Locate every uninfected red blood cell.
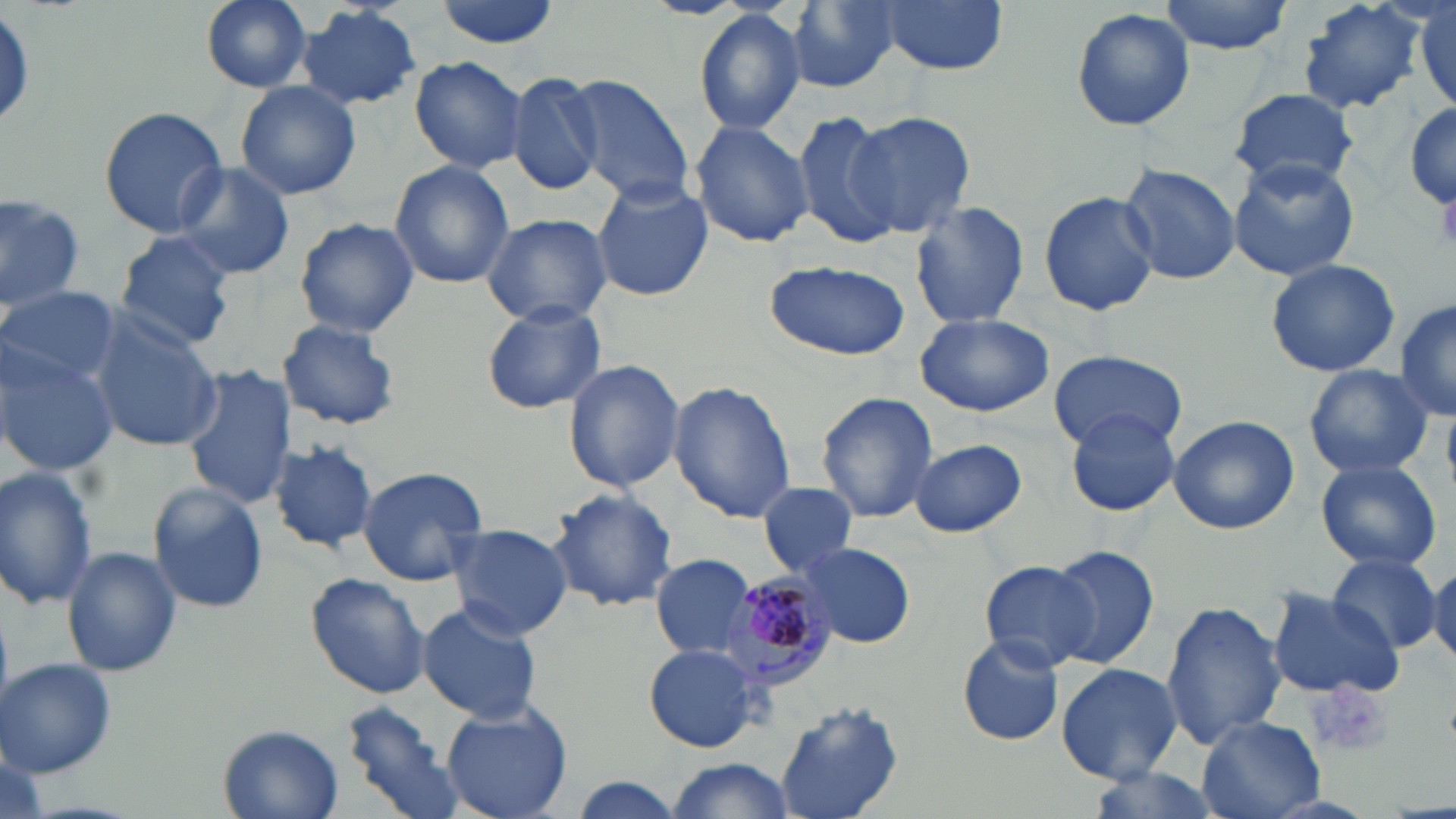
Approximate bounding boxes as named x1/y1/x2/y2 corners in pixels.
Uninfected red blood cells: (x1=197, y1=0, x2=315, y2=93), (x1=434, y1=0, x2=560, y2=49), (x1=639, y1=0, x2=756, y2=21), (x1=784, y1=0, x2=898, y2=93), (x1=877, y1=0, x2=1008, y2=74), (x1=1159, y1=0, x2=1293, y2=54), (x1=1295, y1=0, x2=1434, y2=116), (x1=1411, y1=2, x2=1454, y2=113), (x1=297, y1=4, x2=425, y2=110), (x1=1069, y1=7, x2=1196, y2=132), (x1=694, y1=10, x2=805, y2=133), (x1=408, y1=57, x2=528, y2=172), (x1=509, y1=72, x2=606, y2=197), (x1=559, y1=74, x2=695, y2=205), (x1=403, y1=77, x2=525, y2=260), (x1=233, y1=81, x2=362, y2=202), (x1=1229, y1=87, x2=1359, y2=191), (x1=1406, y1=103, x2=1456, y2=212), (x1=99, y1=106, x2=227, y2=237), (x1=795, y1=110, x2=903, y2=250), (x1=848, y1=112, x2=978, y2=238), (x1=690, y1=118, x2=814, y2=248), (x1=1228, y1=158, x2=1361, y2=281), (x1=387, y1=161, x2=515, y2=288), (x1=170, y1=163, x2=297, y2=280), (x1=1120, y1=164, x2=1241, y2=285), (x1=590, y1=177, x2=713, y2=302), (x1=1039, y1=189, x2=1160, y2=317), (x1=0, y1=192, x2=83, y2=311), (x1=911, y1=201, x2=1029, y2=330), (x1=480, y1=213, x2=613, y2=328), (x1=295, y1=217, x2=420, y2=337), (x1=112, y1=231, x2=237, y2=350), (x1=1265, y1=257, x2=1400, y2=378), (x1=765, y1=259, x2=911, y2=362), (x1=2, y1=285, x2=120, y2=389), (x1=1394, y1=295, x2=1455, y2=423), (x1=482, y1=300, x2=607, y2=414), (x1=87, y1=310, x2=224, y2=451), (x1=915, y1=310, x2=1055, y2=417), (x1=277, y1=319, x2=402, y2=430), (x1=1, y1=347, x2=118, y2=476), (x1=1049, y1=349, x2=1187, y2=453), (x1=562, y1=357, x2=685, y2=493), (x1=181, y1=364, x2=296, y2=510), (x1=1304, y1=364, x2=1433, y2=479), (x1=668, y1=380, x2=796, y2=523), (x1=817, y1=389, x2=939, y2=523), (x1=1065, y1=409, x2=1179, y2=516), (x1=1167, y1=413, x2=1299, y2=535), (x1=267, y1=438, x2=377, y2=553), (x1=910, y1=439, x2=1027, y2=538), (x1=1315, y1=458, x2=1443, y2=571), (x1=354, y1=465, x2=491, y2=585), (x1=0, y1=467, x2=100, y2=610), (x1=757, y1=481, x2=858, y2=578), (x1=147, y1=484, x2=269, y2=614), (x1=545, y1=488, x2=678, y2=614), (x1=444, y1=522, x2=572, y2=640), (x1=796, y1=543, x2=915, y2=648), (x1=1047, y1=544, x2=1160, y2=668), (x1=62, y1=546, x2=182, y2=678), (x1=653, y1=552, x2=757, y2=659), (x1=1323, y1=552, x2=1442, y2=656), (x1=979, y1=559, x2=1099, y2=672), (x1=1429, y1=565, x2=1456, y2=664), (x1=304, y1=572, x2=432, y2=699), (x1=1267, y1=588, x2=1404, y2=699), (x1=415, y1=601, x2=544, y2=725), (x1=1161, y1=601, x2=1287, y2=749), (x1=955, y1=636, x2=1064, y2=747), (x1=644, y1=643, x2=763, y2=752), (x1=2, y1=657, x2=117, y2=777), (x1=1056, y1=662, x2=1181, y2=782), (x1=439, y1=700, x2=572, y2=818), (x1=771, y1=700, x2=905, y2=819), (x1=340, y1=701, x2=461, y2=819), (x1=1198, y1=718, x2=1324, y2=818), (x1=218, y1=724, x2=344, y2=819), (x1=663, y1=760, x2=797, y2=818), (x1=1082, y1=766, x2=1227, y2=819), (x1=571, y1=777, x2=686, y2=819).

Summary:
  - Platelet locations: (x1=1436, y1=186, x2=1456, y2=253), (x1=1314, y1=684, x2=1395, y2=757)
  - Plasmodium malariae-infected red blood cell locations: (x1=722, y1=571, x2=835, y2=689)
  - Slide-level diagnosis: Plasmodium malariae
  - Magnification: 1000x
  - Modality: optical microscopy
  - Preparation: thin blood film
  - Image size: 1456×819 pixels
  - Field of view: single
  - Stain: May-Grünwald-Giemsa